Report the malaria status of this cell.
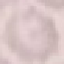

Uninfected.

stain = Giemsa
preparation = thin smear
image type = cell patch, automatically extracted from a larger field of view and resized to 64 × 64 pixels
capture = smartphone through the microscope eyepiece